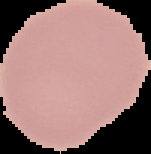
Summary:
  - Image size: 151×154 pixels
  - Preparation: thin blood film
  - Malaria status: uninfected
  - Image type: segmented cell region on a black background